Name the parasite shown.
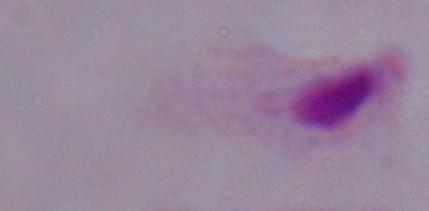

A trichomonad.

Micrograph. 1000x magnification.